Assess this cell for malaria.
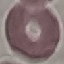

It is uninfected.

Summary:
  - Capture: smartphone through the microscope eyepiece
  - Stain: Giemsa
  - Preparation: thin blood smear
  - Image type: automatically extracted cell patch, resized to 64 × 64 pixels